Outline each blood parasite and name the species.
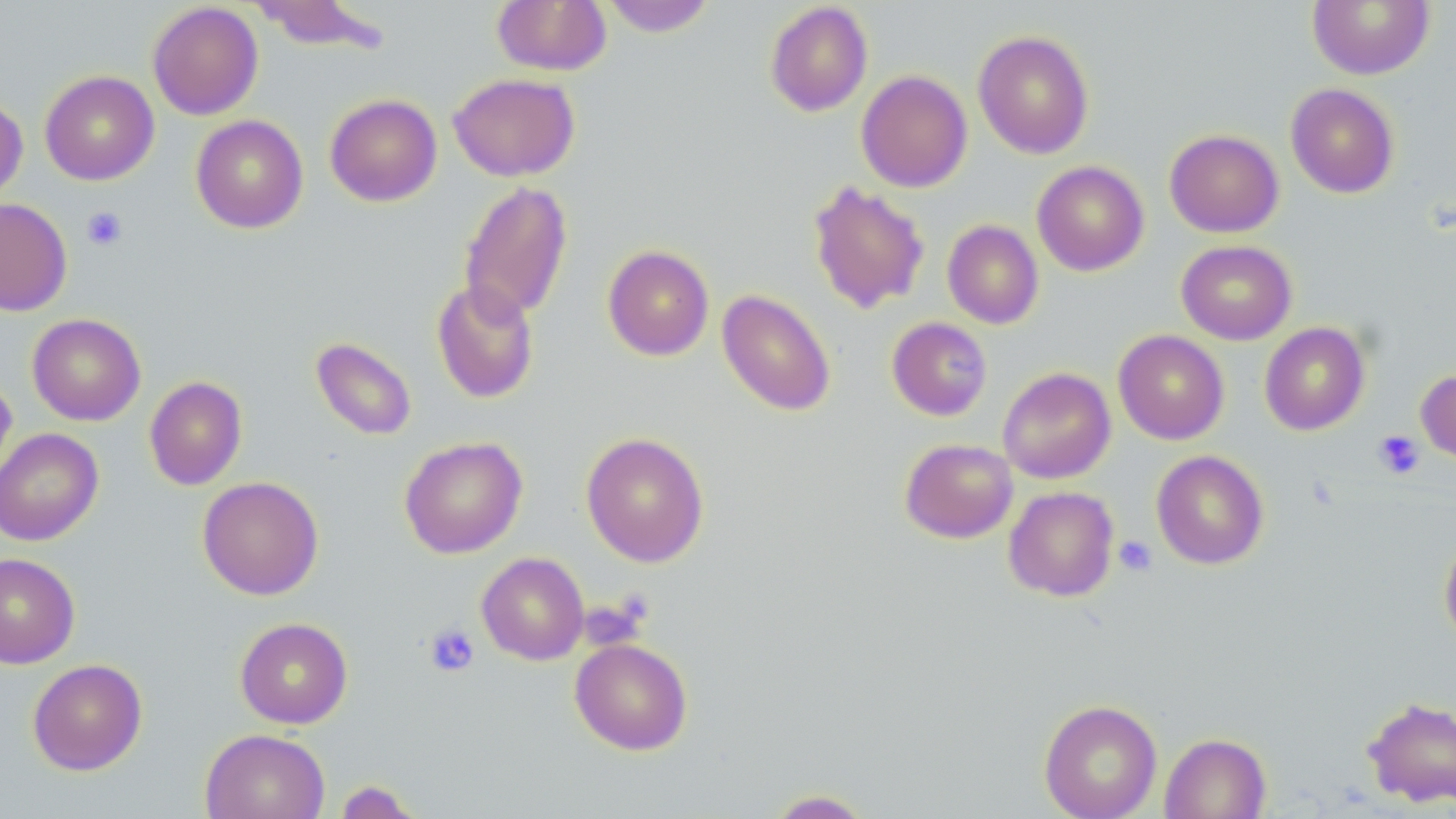

No blood parasites observed.

slide-level diagnosis = negative for blood parasites
magnification = 1000x
image size = 1456×819 pixels
platelet locations = approximate bounding boxes as (x1, y1, x2, y2) in pixels: (81, 206, 127, 251), (1373, 430, 1425, 479), (1114, 536, 1157, 576), (424, 623, 480, 677)
modality = optical microscopy
preparation = thin blood smear
field of view = single
stain = May-Grünwald-Giemsa
uninfected red blood cell locations = approximate bounding boxes as (x1, y1, x2, y2) in pixels: (249, 0, 391, 54), (492, 0, 611, 76), (600, 0, 717, 37), (764, 1, 874, 117), (1307, 1, 1435, 80), (147, 2, 264, 120), (973, 29, 1094, 159), (40, 70, 159, 186), (856, 70, 973, 193), (448, 73, 580, 181), (1285, 83, 1400, 199), (324, 93, 442, 207), (0, 94, 27, 203), (190, 115, 309, 234), (1164, 129, 1284, 237), (1032, 160, 1149, 276), (458, 180, 573, 324), (807, 180, 930, 315), (0, 198, 72, 316), (942, 220, 1044, 329), (1176, 240, 1296, 345), (602, 245, 714, 361), (430, 280, 540, 404), (716, 289, 836, 417), (27, 313, 146, 426), (887, 317, 993, 420), (1259, 322, 1370, 435), (1113, 329, 1229, 445), (311, 337, 417, 441), (998, 367, 1116, 484), (1416, 368, 1456, 464), (0, 372, 17, 492), (144, 375, 247, 490), (0, 427, 104, 546), (581, 431, 710, 567), (399, 436, 528, 559), (900, 438, 1018, 543), (1151, 450, 1269, 570), (197, 476, 324, 600), (1003, 486, 1119, 601), (1439, 534, 1456, 649), (476, 551, 590, 665), (0, 553, 80, 669), (234, 617, 353, 728), (569, 638, 693, 755), (27, 658, 147, 775), (1362, 697, 1456, 809), (1038, 699, 1162, 819), (200, 728, 330, 819), (1159, 732, 1271, 819), (333, 779, 425, 819), (763, 789, 875, 818)